Classify this cell by malaria status.
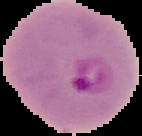
Parasitized.

Cell region segmented out of the field of view; the surrounding area is masked to black. Image is 142×136 pixels. From a thin blood film.